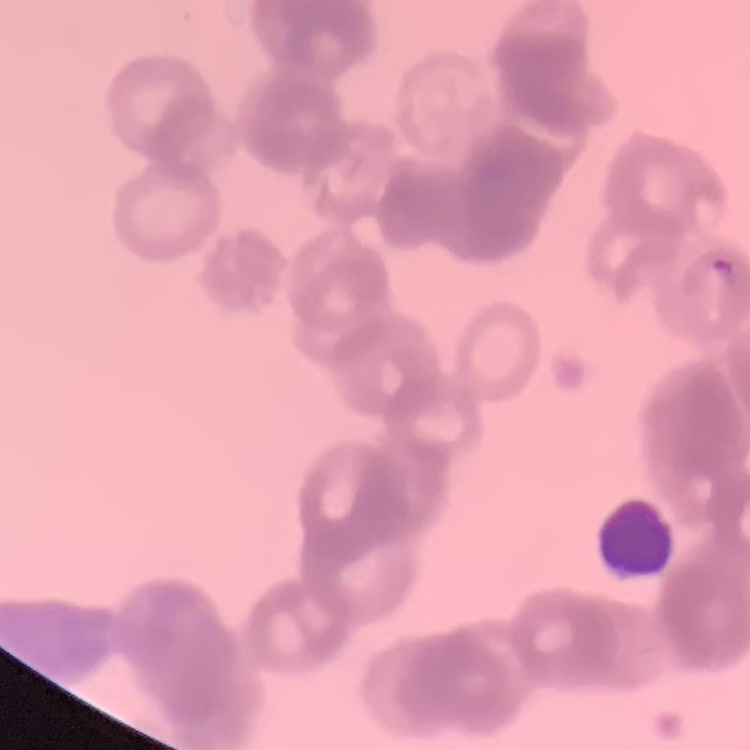

Summary:
  - Erythrocyte morphology: rouleaux formation
  - Stain: Field's or Giemsa
  - Image type: one tile cut from a larger photomicrograph
  - Preparation: thin blood film